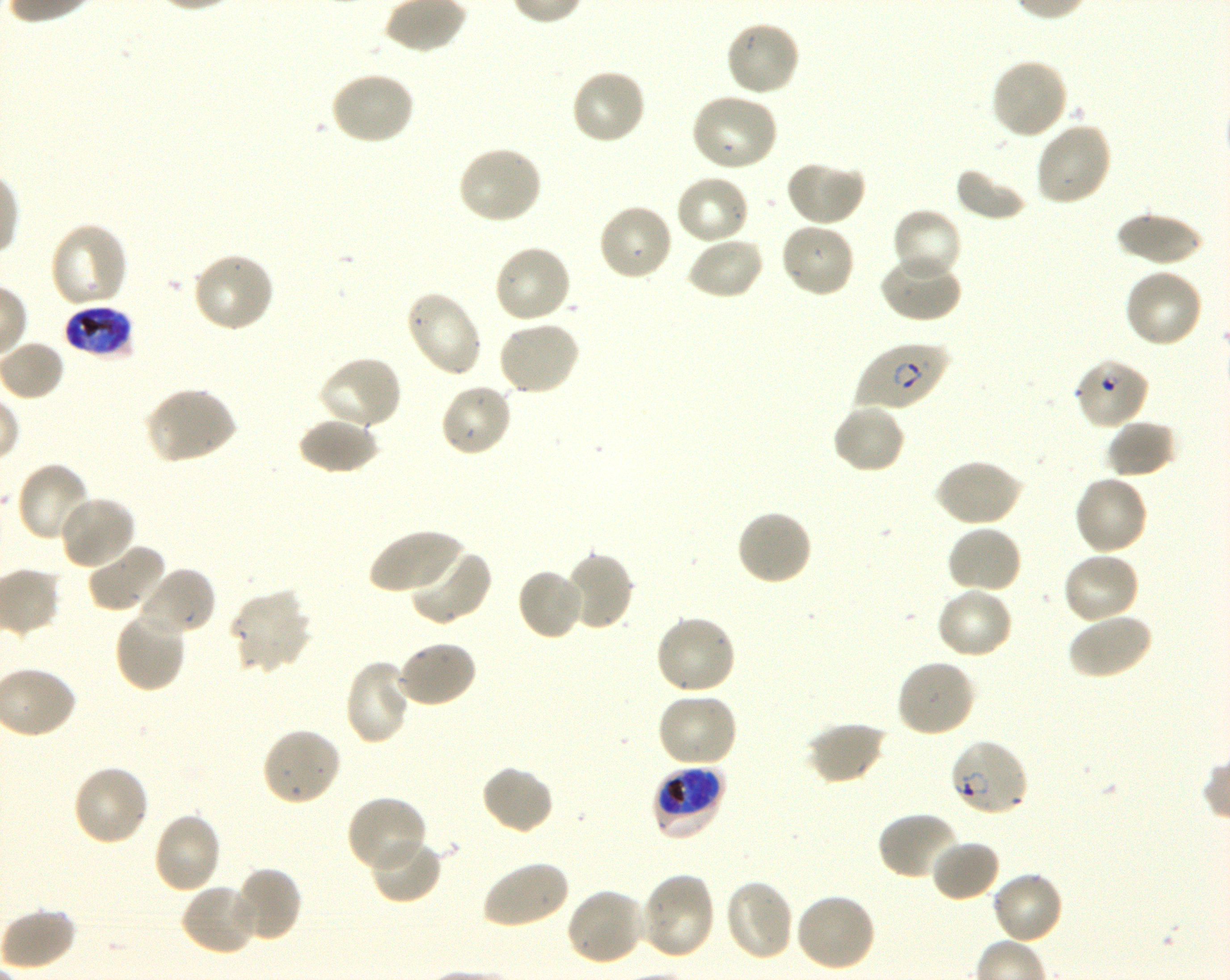

Not every red blood cell is marked. A life-cycle stage — or a range of stages, where the recorded stages span more than one — follows each staged infected red blood cell.
{
  "field_of_view": "single",
  "locations_of_infected_red_blood_cells": "approximate bounding rectangles given as corner coordinates in pixels from the top-left: (x1=64, y1=304, x2=134, y2=359) late trophozoite to early schizont; (x1=856, y1=340, x2=950, y2=412) early ring to early trophozoite; (x1=948, y1=739, x2=1029, y2=819) ring; (x1=651, y1=764, x2=727, y2=842) early trophozoite to early schizont",
  "locations_of_uninfected_red_blood_cells": "approximate bounding rectangles given as corner coordinates in pixels from the top-left: (x1=723, y1=19, x2=801, y2=98), (x1=990, y1=58, x2=1069, y2=141), (x1=569, y1=68, x2=648, y2=146), (x1=329, y1=71, x2=416, y2=147), (x1=689, y1=92, x2=780, y2=173), (x1=1033, y1=120, x2=1113, y2=206), (x1=457, y1=145, x2=544, y2=226), (x1=785, y1=159, x2=866, y2=227), (x1=955, y1=167, x2=1030, y2=222), (x1=674, y1=173, x2=750, y2=246), (x1=597, y1=202, x2=674, y2=282), (x1=891, y1=207, x2=963, y2=283), (x1=1116, y1=211, x2=1203, y2=267), (x1=779, y1=220, x2=857, y2=299), (x1=49, y1=221, x2=130, y2=310), (x1=685, y1=236, x2=765, y2=300), (x1=493, y1=244, x2=573, y2=325), (x1=191, y1=250, x2=276, y2=334), (x1=878, y1=250, x2=962, y2=323), (x1=1122, y1=268, x2=1204, y2=349), (x1=403, y1=289, x2=484, y2=378), (x1=497, y1=319, x2=581, y2=396), (x1=316, y1=355, x2=403, y2=432), (x1=439, y1=382, x2=513, y2=458), (x1=144, y1=386, x2=237, y2=465), (x1=831, y1=402, x2=906, y2=474), (x1=298, y1=414, x2=380, y2=474), (x1=1105, y1=418, x2=1177, y2=478), (x1=933, y1=458, x2=1024, y2=528), (x1=17, y1=461, x2=93, y2=545), (x1=1073, y1=474, x2=1150, y2=555), (x1=58, y1=495, x2=137, y2=571), (x1=736, y1=508, x2=813, y2=587), (x1=945, y1=524, x2=1023, y2=595), (x1=369, y1=528, x2=465, y2=599), (x1=87, y1=541, x2=168, y2=614), (x1=409, y1=546, x2=493, y2=626), (x1=1061, y1=551, x2=1141, y2=625), (x1=562, y1=552, x2=635, y2=632), (x1=135, y1=566, x2=217, y2=638), (x1=516, y1=566, x2=587, y2=641), (x1=935, y1=586, x2=1014, y2=660), (x1=228, y1=589, x2=312, y2=675), (x1=114, y1=610, x2=188, y2=692), (x1=1067, y1=612, x2=1154, y2=680), (x1=654, y1=613, x2=737, y2=696), (x1=394, y1=639, x2=477, y2=708), (x1=344, y1=658, x2=413, y2=747), (x1=896, y1=658, x2=977, y2=739), (x1=656, y1=691, x2=739, y2=768), (x1=806, y1=721, x2=887, y2=785), (x1=261, y1=727, x2=342, y2=807), (x1=480, y1=763, x2=554, y2=836), (x1=72, y1=765, x2=151, y2=848), (x1=346, y1=795, x2=428, y2=874), (x1=151, y1=811, x2=223, y2=895), (x1=875, y1=811, x2=962, y2=883), (x1=369, y1=836, x2=443, y2=904), (x1=931, y1=837, x2=1000, y2=902), (x1=480, y1=859, x2=569, y2=930), (x1=229, y1=867, x2=303, y2=944), (x1=990, y1=869, x2=1064, y2=945), (x1=639, y1=871, x2=717, y2=961), (x1=724, y1=879, x2=796, y2=963), (x1=180, y1=882, x2=261, y2=957), (x1=564, y1=886, x2=646, y2=966), (x1=794, y1=892, x2=876, y2=973), (x1=1, y1=907, x2=77, y2=971)",
  "stain": "Giemsa",
  "image_size": "1230×980 pixels",
  "donor_blood_group": "O+",
  "culture": "P. falciparum strain 3D7, shaking, in vitro",
  "objective": "100x, oil immersion, numerical aperture 1.30",
  "locations_of_red_blood_cells_of_indeterminate_infection_status": "approximate bounding rectangles given as corner coordinates in pixels from the top-left: (x1=1072, y1=357, x2=1150, y2=430)",
  "preparation": "thin blood smear"
}